State which parasite is depicted.
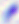
This is Toxoplasma gondii.

modality: photomicrograph
magnification: 400x